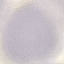

malaria status = uninfected
image type = cell patch, automatically extracted from a larger field of view and resized to 64 × 64 pixels
preparation = thin smear
stain = Giemsa
capture = smartphone camera at the microscope eyepiece